Assess this cell for malaria.
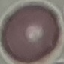

Uninfected.

image type = automatically extracted cell patch, resized to 64 × 64 pixels
stain = Giemsa
capture = smartphone camera at the microscope eyepiece
preparation = thin smear